Assess this cell for malaria.
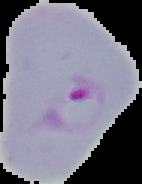

It is parasitized.

Image is 142×184 pixels. The area outside the segmented cell region is set to black. From a thin blood film.